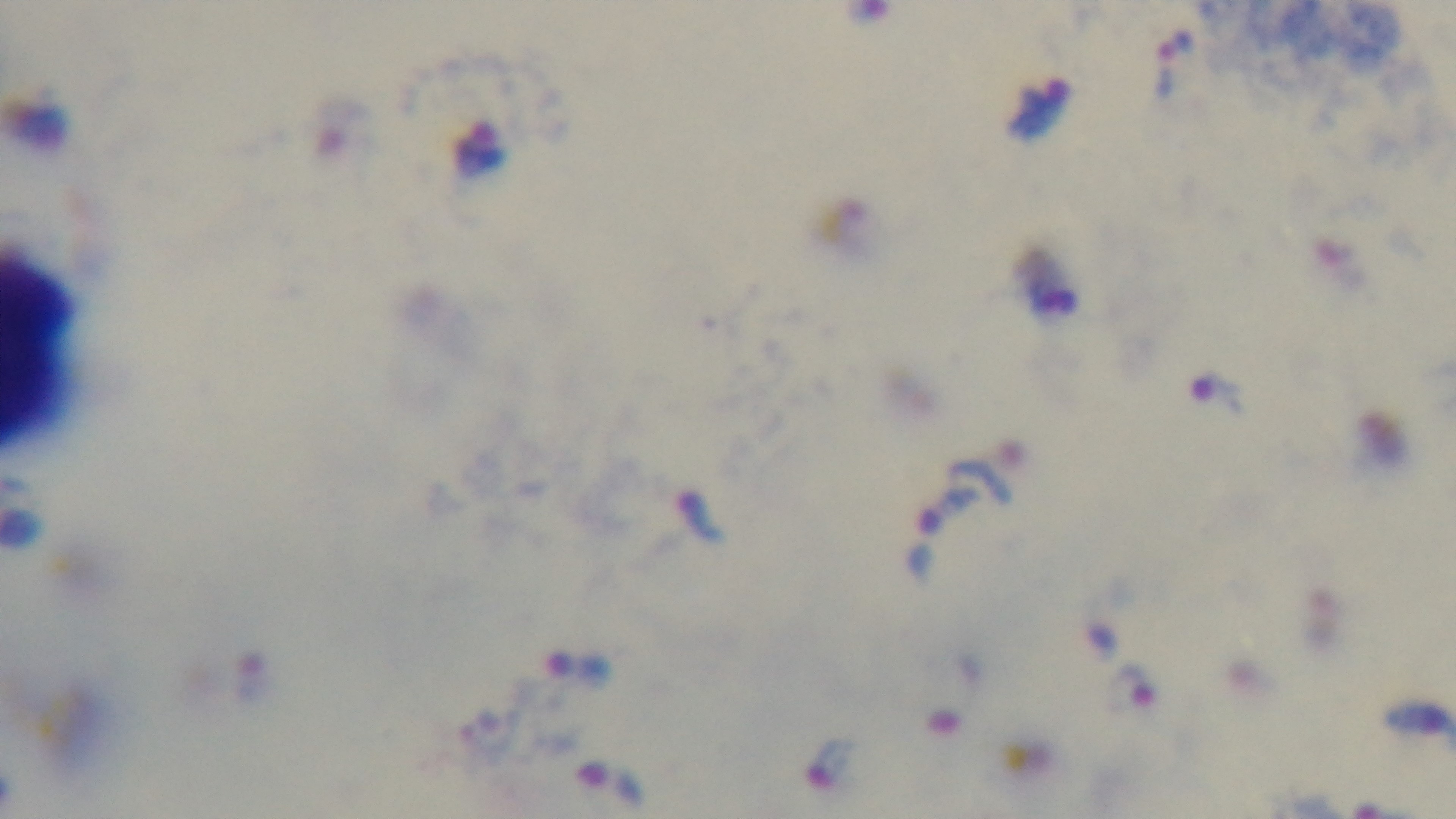
Summary:
  - Capture: mounted 4K digital camera
  - Stain: Giemsa
  - Preparation: thick
  - Modality: light microscopy
  - Field of view: single
  - Objective: 100x oil immersion
  - Malaria status: positive